Assess this cell for malaria.
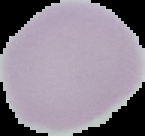
Uninfected.

Summary:
  - Image type: segmented cell region on a black background
  - Preparation: thin blood smear
  - Image size: 145×136 pixels